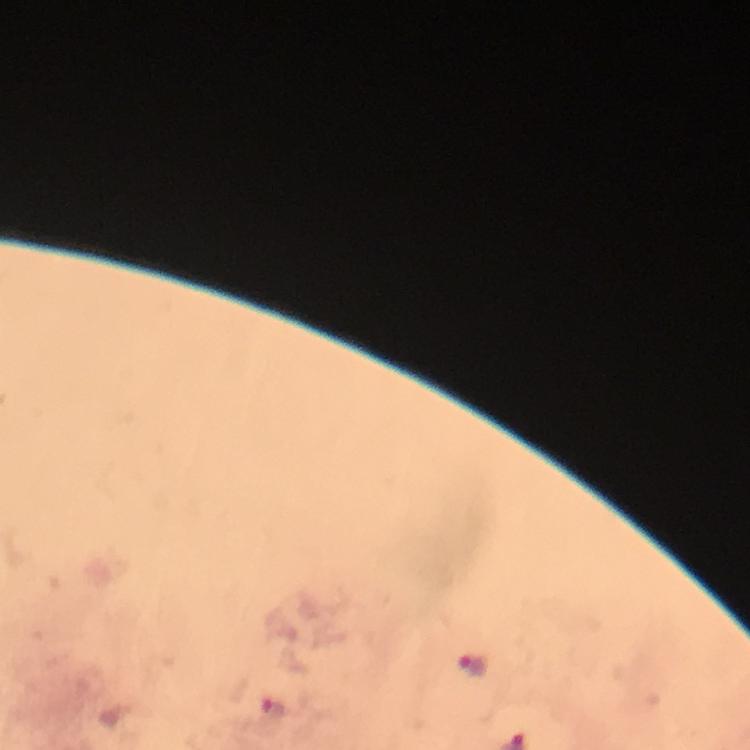

Approximate centers as (x, y) in pixels.
Summary:
  - Malaria parasite locations: (472, 664)
  - Preparation: thick blood film
  - Cropped from: one field of view
  - Context: from a malaria diagnostic workup
  - Immersion oil: used
  - Magnification: 100x
  - Capture: smartphone photograph through a microscope
  - Stain: Giemsa
  - Image size: 750×750 pixels